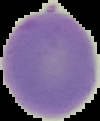

preparation = thin blood smear
image type = segmented cell region on a black background
result = no Plasmodium parasites detected
image size = 100×121 pixels